Outline platelets.
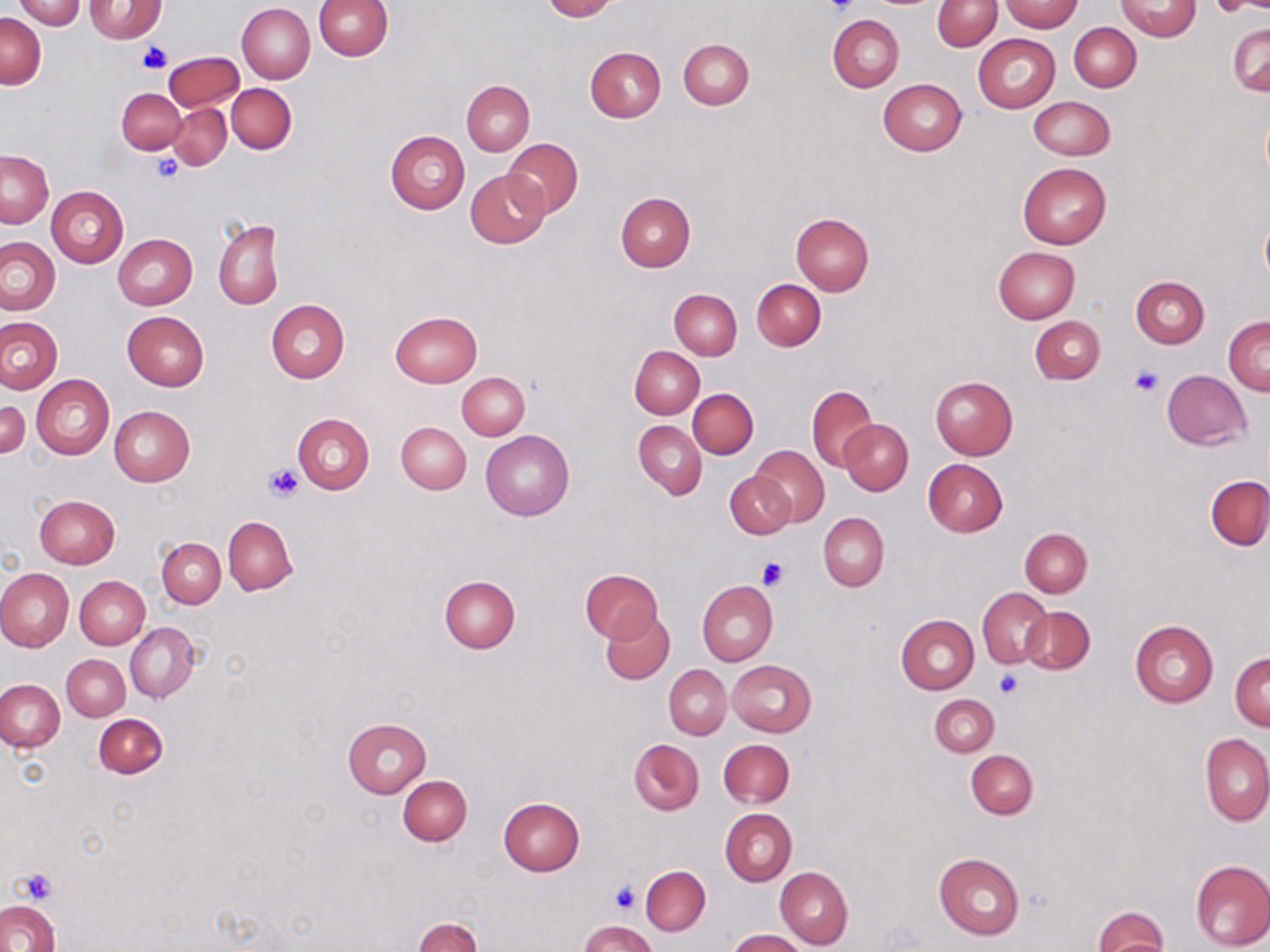

Approximate bounding boxes as [x1, y1, x2, y2] in pixels.
Platelets: [824, 0, 861, 18], [138, 43, 171, 74], [152, 155, 184, 183], [1130, 366, 1162, 397], [263, 462, 306, 502], [757, 555, 788, 590], [994, 669, 1023, 699], [17, 868, 56, 904], [609, 882, 640, 915].

{
  "slide_level_diagnosis": "no evidence of blood parasites",
  "image_size": "1270×952 pixels",
  "magnification": "1000x",
  "modality": "optical microscopy",
  "uninfected_red_blood_cell_locations": "approximate bounding boxes as [x1, y1, x2, y2] in pixels: [13, 0, 87, 29], [314, 0, 393, 60], [540, 0, 617, 21], [1205, 0, 1269, 15], [84, 1, 165, 42], [933, 1, 1001, 51], [999, 1, 1083, 32], [1117, 1, 1201, 40], [237, 3, 315, 83], [0, 13, 46, 89], [828, 14, 904, 92], [1069, 22, 1141, 92], [1228, 23, 1269, 96], [973, 34, 1060, 112], [679, 39, 754, 110], [584, 47, 665, 122], [164, 51, 243, 111], [462, 80, 534, 155], [879, 80, 967, 155], [226, 83, 297, 154], [117, 89, 186, 154], [1027, 96, 1114, 160], [168, 103, 231, 170], [385, 129, 469, 215], [502, 138, 582, 217], [1, 150, 53, 227], [1018, 163, 1111, 248], [466, 171, 548, 249], [47, 186, 128, 266], [615, 192, 696, 272], [791, 213, 873, 295], [1260, 214, 1270, 288], [214, 217, 284, 310], [114, 235, 197, 310], [1, 238, 61, 314], [993, 246, 1081, 323], [1130, 276, 1209, 348], [752, 279, 825, 349], [670, 288, 741, 360], [265, 299, 350, 383], [122, 311, 209, 392], [389, 311, 481, 388], [1224, 315, 1269, 394], [1029, 316, 1105, 384], [0, 317, 63, 393], [631, 347, 704, 419], [1162, 371, 1251, 449], [457, 373, 530, 440], [32, 374, 114, 460], [930, 376, 1018, 459], [807, 385, 878, 471], [688, 388, 758, 458], [0, 399, 30, 460], [109, 406, 195, 487], [292, 413, 375, 494], [634, 420, 706, 499], [840, 420, 913, 494], [397, 421, 471, 494], [481, 428, 574, 520], [748, 445, 830, 528], [923, 459, 1007, 536], [725, 471, 795, 539], [1206, 475, 1270, 550], [34, 495, 120, 569], [818, 513, 888, 590], [224, 516, 298, 595], [1019, 527, 1092, 597], [158, 538, 225, 608], [0, 568, 74, 653], [581, 569, 663, 643], [76, 576, 150, 649], [440, 576, 520, 652], [697, 579, 778, 667], [978, 588, 1052, 668], [1020, 607, 1095, 674], [600, 611, 674, 686], [896, 615, 979, 694], [1129, 620, 1219, 707], [125, 622, 200, 703], [1230, 653, 1269, 730], [62, 654, 129, 720], [727, 660, 817, 736], [664, 665, 732, 739], [0, 679, 64, 752], [929, 694, 999, 757], [94, 714, 167, 778], [342, 718, 431, 797], [1200, 733, 1270, 826], [629, 739, 703, 815], [720, 739, 794, 808], [966, 750, 1038, 819], [399, 775, 472, 845], [498, 797, 585, 875], [720, 808, 796, 885], [933, 853, 1024, 939], [1189, 860, 1270, 951], [641, 866, 710, 936], [775, 866, 853, 950], [0, 900, 60, 952], [1094, 906, 1168, 952], [412, 917, 481, 952], [580, 920, 657, 951], [727, 929, 805, 952]",
  "preparation": "thin blood smear",
  "stain": "May-Grünwald-Giemsa",
  "field_of_view": "one of a larger specimen"
}